Point out Plasmodium parasites and leukocytes.
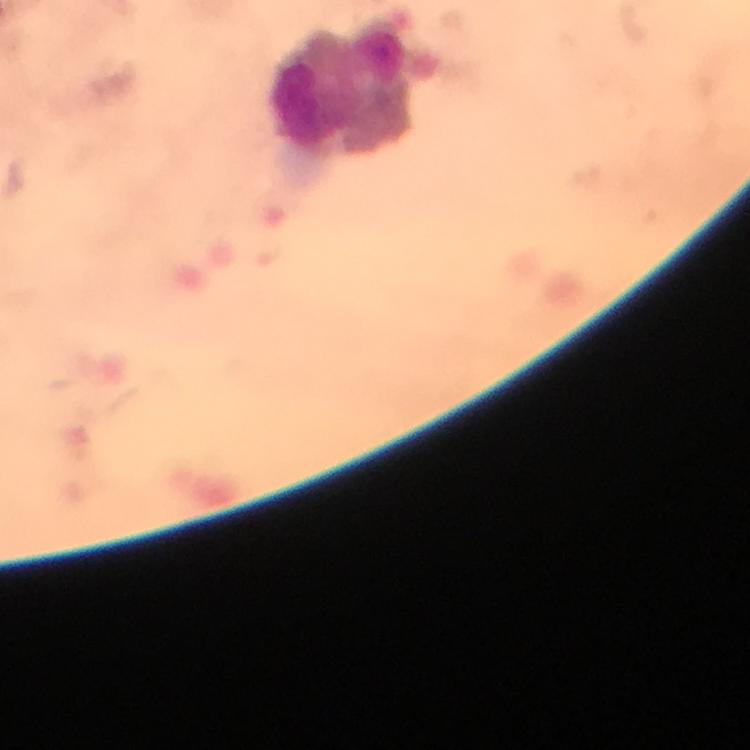

No Plasmodium parasites seen.
Approximate object centers, in pixels from the top-left corner.
Leukocytes: (x=342, y=86).

Summary:
  - Image size: 750×750 pixels
  - Preparation: thick blood smear
  - Capture: smartphone camera through the microscope
  - Context: from a malaria diagnostic workup
  - Immersion oil: applied
  - Magnification: 100x
  - Cropped from: a single field of view
  - Stain: Giemsa